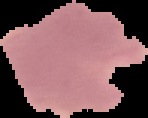

image size = 148×118 pixels
preparation = thin blood smear
image type = segmented cell region with the area outside set to black
result = Plasmodium parasites detected